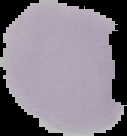
Image is 127×136 pixels. Cell region segmented out of the field of view; the surrounding area is masked to black. From a thin blood smear. Malaria status: uninfected.